Classify this cell by malaria status.
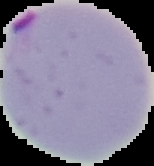

Parasitized.

preparation = thin blood smear
image type = segmented cell region on a black background
image size = 154×166 pixels